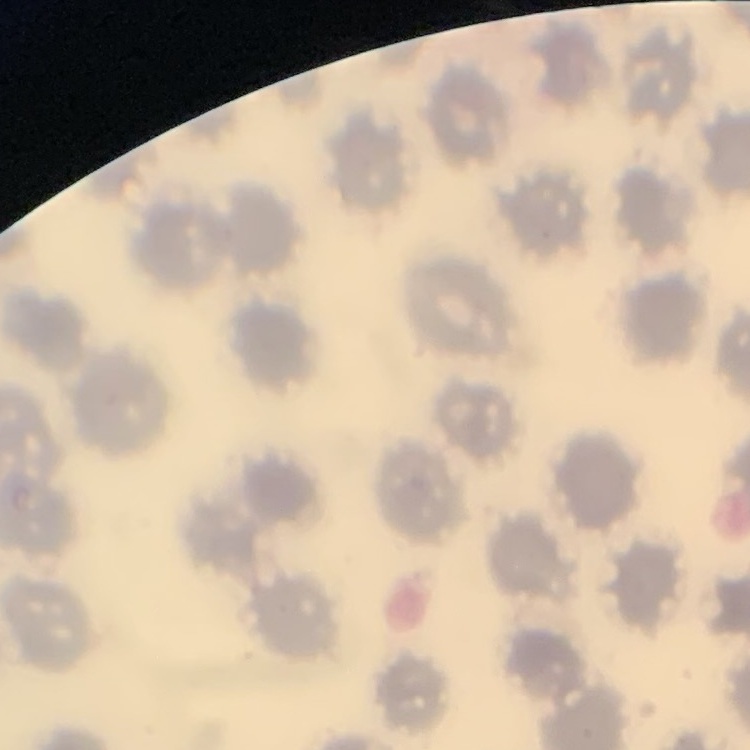

{
  "erythrocyte_morphology": "no rouleaux formation",
  "stain": "Field's or Giemsa",
  "preparation": "thin blood smear",
  "image_type": "square crop of a larger photomicrograph"
}